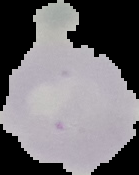
preparation = thin blood film
image type = segmented cell region on a black background
result = negative for Plasmodium parasites
image size = 139×175 pixels